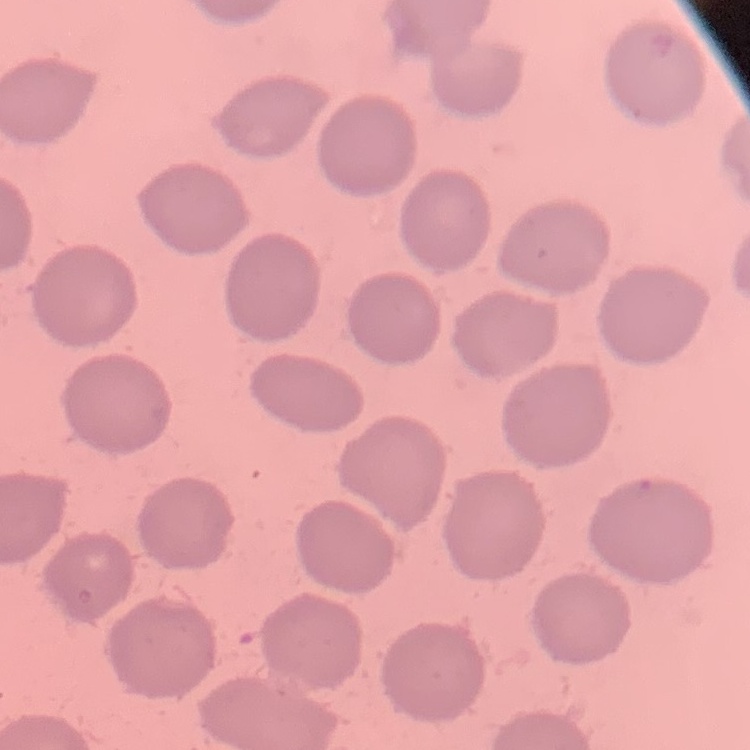
red blood cell morphology = no rouleaux formation
image type = one tile cut from a larger photomicrograph
stain = Field's or Giemsa
preparation = thin blood smear